State which parasite is depicted.
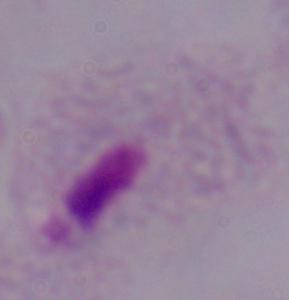
A trichomonad.

Captured at 1000x magnification. Photomicrograph.